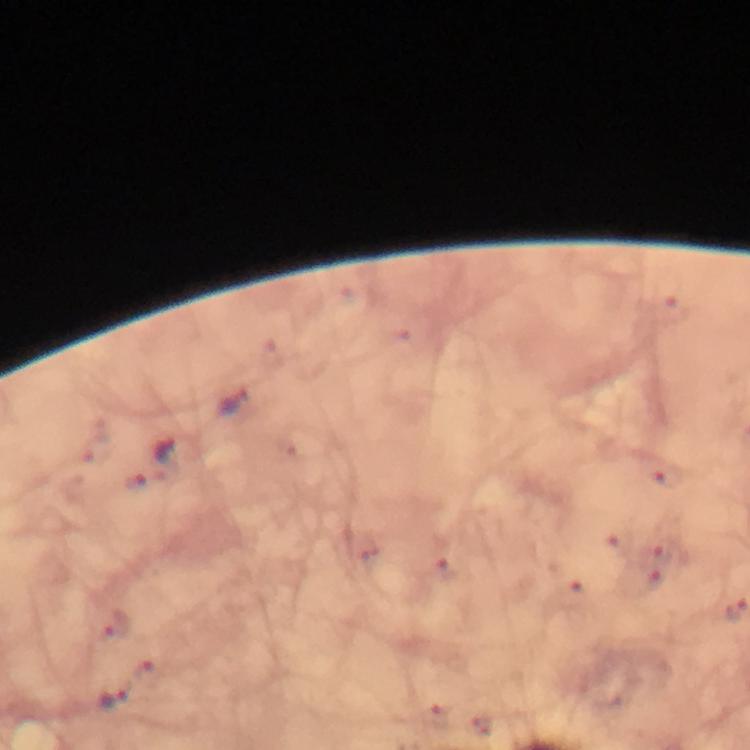 Approximate centers as {x, y} in pixels. Plasmodium parasite locations: {675, 308}, {231, 402}, {167, 451}, {667, 477}, {135, 484}, {448, 568}, {572, 596}, {114, 623}, {112, 697}. Thick smear. At 100x magnification. Immersion oil was used. From a diagnostic examination for malaria. A crop from one field of view. Giemsa-stained preparation. Image is 750×750 pixels. Photographed with a smartphone mounted on the microscope.